Locate every blood parasite and identify its species.
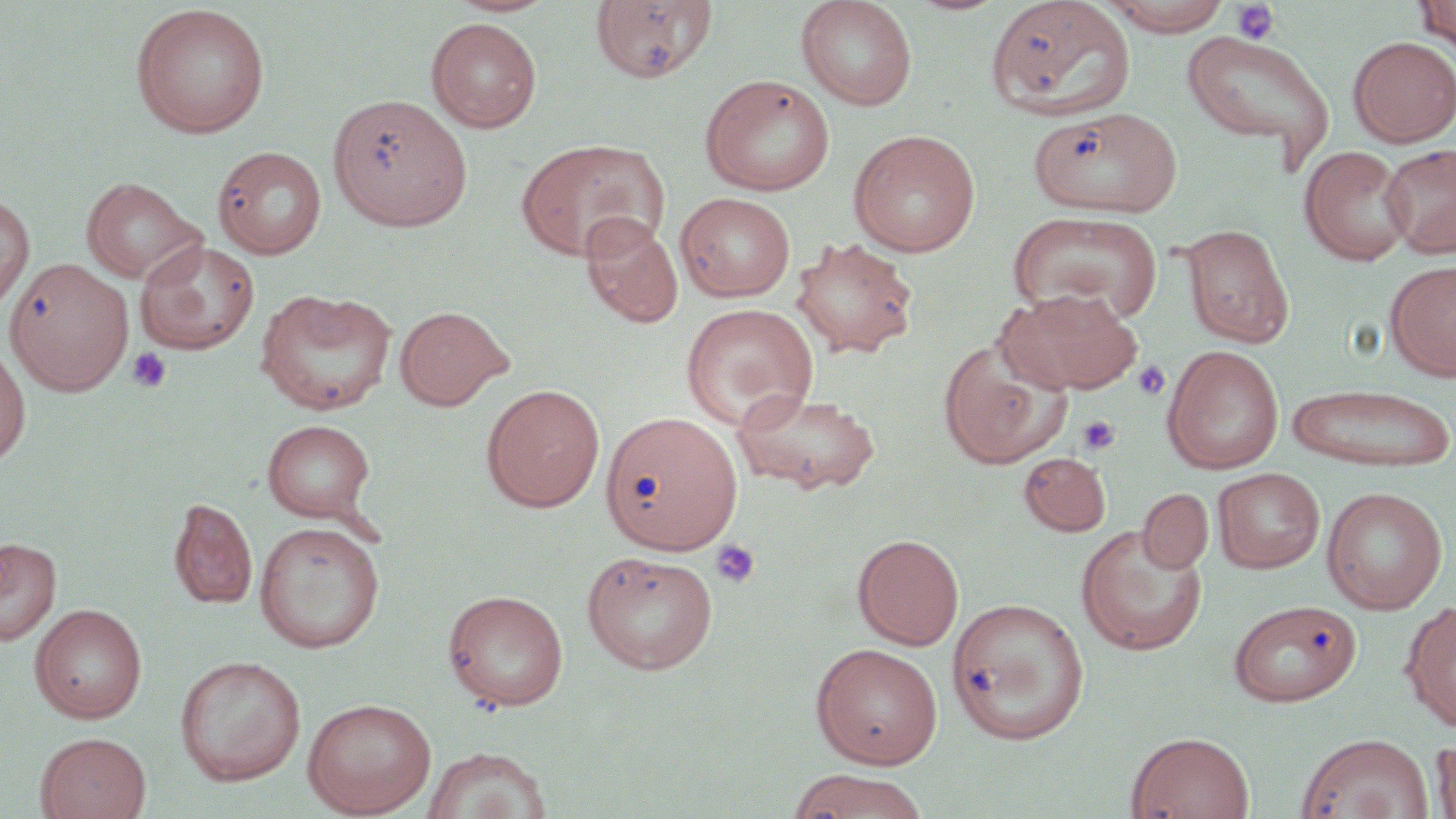
No blood parasites seen.

Summary:
  - Coordinate format: approximate bounding boxes as (x1, y1, x2, y2) in pixels
  - Platelet locations: (1230, 1, 1280, 46), (126, 347, 171, 393), (1131, 359, 1170, 401), (1077, 415, 1120, 456), (710, 539, 762, 589)
  - Uninfected red blood cell locations: (444, 0, 558, 17), (795, 0, 918, 111), (985, 0, 1136, 122), (1099, 0, 1236, 35), (1415, 0, 1456, 58), (590, 1, 718, 84), (130, 4, 270, 139), (426, 17, 542, 132), (1181, 31, 1335, 164), (1368, 35, 1456, 261), (1348, 36, 1456, 147), (700, 74, 836, 196), (328, 94, 472, 231), (1029, 106, 1182, 216), (848, 130, 982, 257), (515, 138, 669, 262), (1381, 143, 1456, 258), (212, 145, 327, 259), (1299, 145, 1414, 266), (80, 176, 205, 284), (675, 191, 797, 302), (0, 192, 35, 314), (1007, 209, 1164, 324), (580, 213, 683, 328), (1180, 223, 1294, 348), (791, 237, 919, 359), (135, 239, 260, 355), (3, 257, 134, 395), (1386, 260, 1456, 380), (254, 288, 397, 416), (1000, 288, 1143, 394), (681, 303, 818, 430), (394, 305, 511, 410), (937, 336, 1072, 469), (0, 341, 32, 470), (1162, 345, 1284, 474), (1286, 381, 1455, 472), (481, 383, 605, 512), (732, 390, 882, 495), (601, 410, 743, 555), (262, 419, 376, 522), (1018, 452, 1111, 536), (1213, 467, 1325, 573), (1321, 486, 1448, 614), (1138, 489, 1213, 573), (169, 497, 258, 610), (254, 521, 385, 653), (1075, 524, 1208, 656), (852, 533, 964, 650), (0, 537, 61, 645), (581, 549, 719, 673), (443, 588, 569, 711), (947, 596, 1090, 745), (1228, 599, 1362, 706), (1401, 601, 1456, 732), (30, 604, 147, 723), (810, 642, 944, 768), (174, 655, 306, 786), (303, 697, 436, 818), (1126, 731, 1255, 818), (36, 732, 151, 819), (1296, 733, 1433, 819), (1432, 736, 1456, 818), (422, 746, 552, 819), (784, 770, 931, 819)
  - Slide-level diagnosis: negative for blood parasites
  - Image size: 1456×819 pixels
  - Field of view: single
  - Magnification: 1000x
  - Modality: light microscopy
  - Stain: May-Grünwald-Giemsa
  - Preparation: thin blood smear